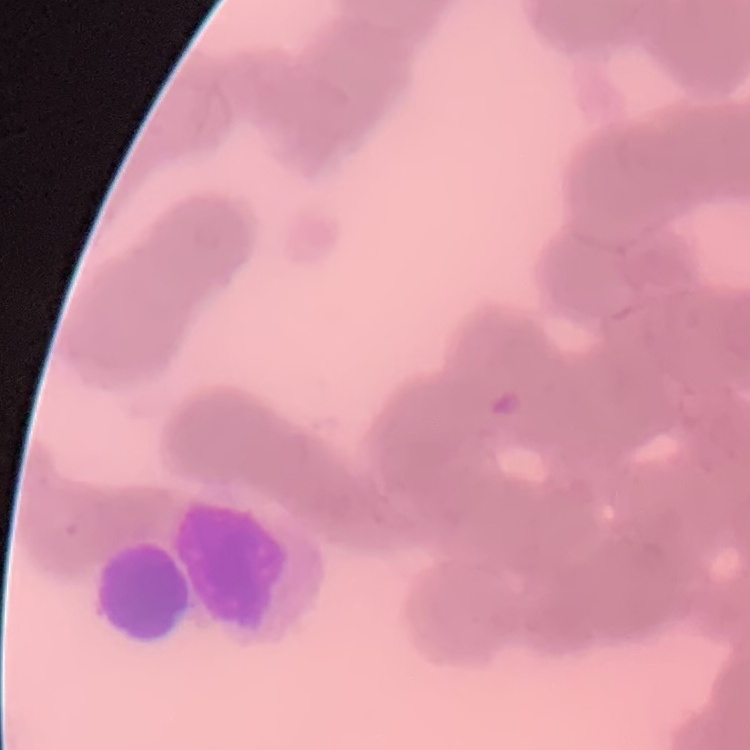
Summary:
  - Erythrocyte morphology: rouleaux formation
  - Preparation: thin blood film
  - Stain: Field's or Giemsa
  - Image type: square crop of a larger photomicrograph